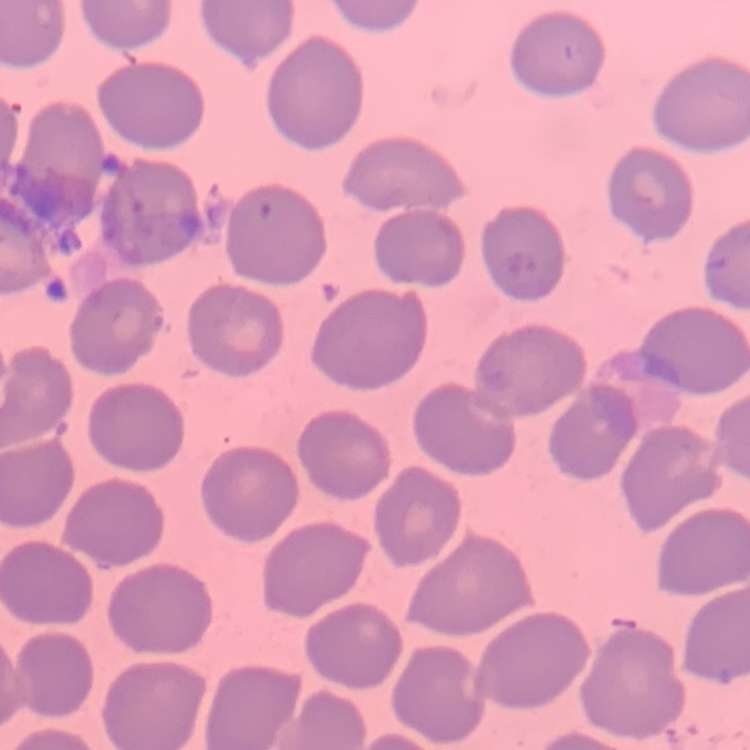 The red blood cells exhibit no rouleaux formation. Square crop of a larger photomicrograph. Field's or Giemsa stain. Thin blood film.